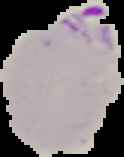
Summary:
  - Image size: 124×157 pixels
  - Image type: segmented cell region on a black background
  - Result: Plasmodium parasites detected
  - Preparation: thin blood smear